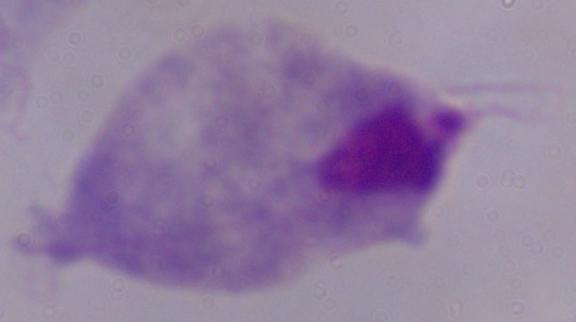

Captured at 1000x magnification. Photomicrograph. A trichomonad is seen.